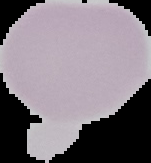

From a thin blood smear. Result: negative for malaria parasites. Segmented cell region on a black background. Image is 151×163 pixels.